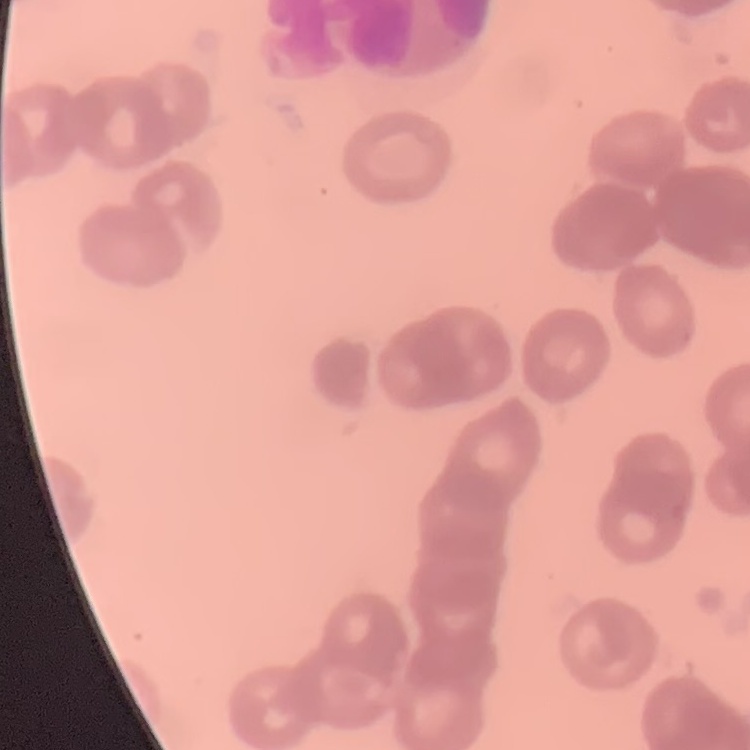

Summary:
  - Red blood cell morphology: rouleaux formation
  - Preparation: thin peripheral smear
  - Stain: Field's or Giemsa
  - Image type: square crop of a larger photomicrograph